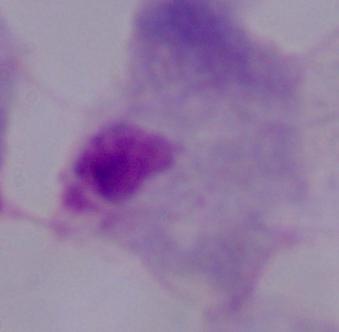

{
  "modality": "micrograph",
  "identification": "trichomonad",
  "magnification": "1000x"
}